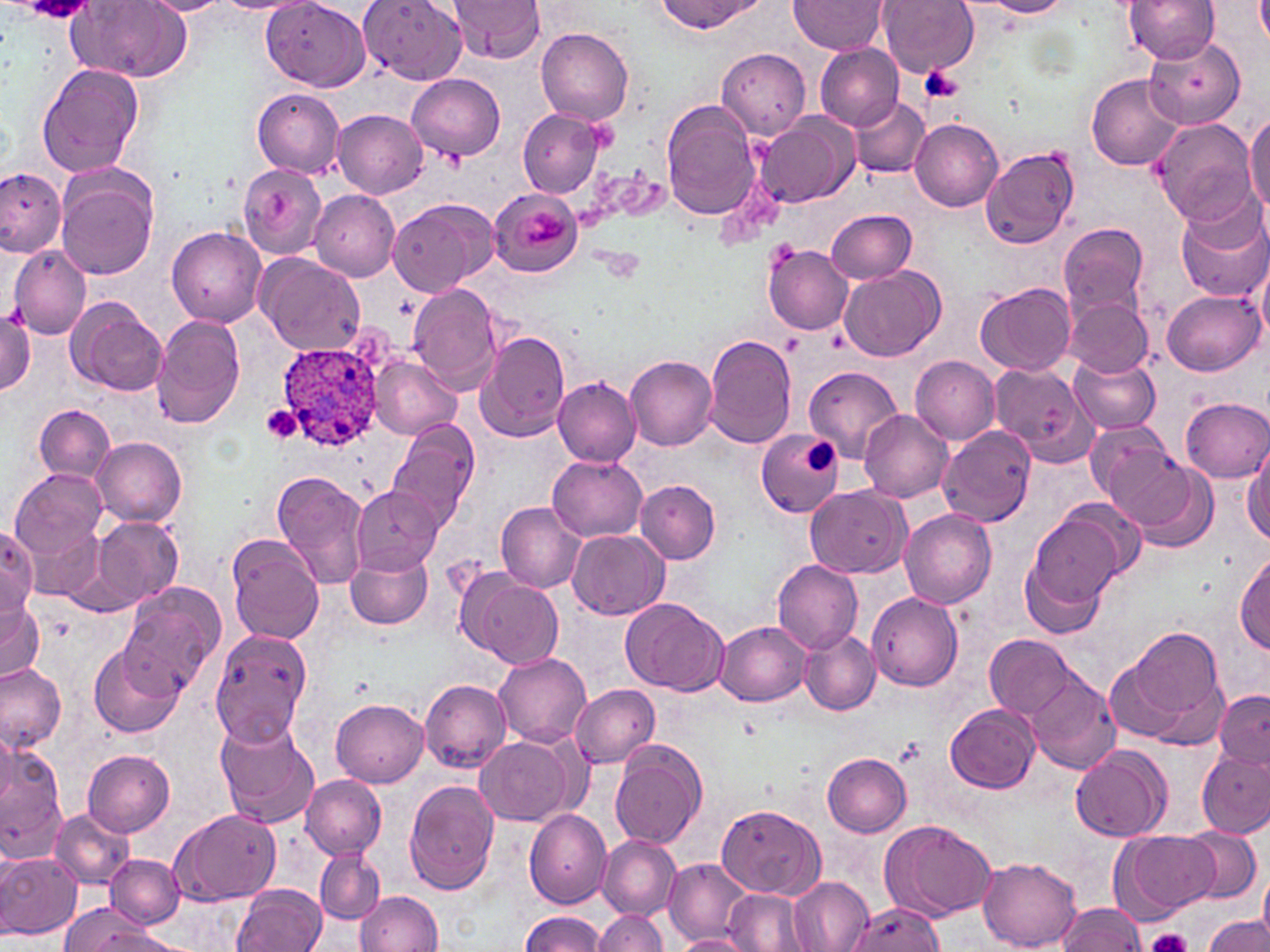

{
  "slide_level_diagnosis": "Plasmodium ovale",
  "stain": "May-Grünwald-Giemsa",
  "plasmodium_ovale_infected_red_blood_cell_locations": "approximate bounding boxes as (x1, y1, x2, y2) in pixels: (271, 339, 382, 450)",
  "uninfected_red_blood_cell_locations": "approximate bounding boxes as (x1, y1, x2, y2) in pixels: (66, 0, 194, 83), (138, 0, 230, 15), (262, 0, 370, 90), (360, 0, 466, 85), (448, 0, 544, 63), (656, 0, 757, 33), (788, 0, 889, 54), (877, 0, 978, 77), (979, 0, 1074, 17), (1122, 0, 1219, 62), (1257, 0, 1270, 49), (213, 1, 313, 12), (535, 27, 634, 124), (1144, 37, 1243, 128), (817, 44, 905, 131), (717, 48, 812, 138), (36, 63, 143, 177), (407, 71, 505, 163), (1086, 74, 1184, 170), (251, 86, 345, 179), (848, 96, 930, 177), (660, 101, 759, 220), (332, 109, 428, 198), (518, 109, 605, 197), (1245, 113, 1270, 216), (757, 114, 859, 210), (1149, 117, 1258, 225), (910, 118, 1004, 212), (979, 145, 1079, 249), (239, 162, 326, 258), (1, 166, 65, 257), (54, 169, 158, 278), (309, 187, 400, 282), (487, 188, 583, 277), (388, 197, 499, 295), (1176, 197, 1270, 302), (825, 208, 917, 283), (1058, 222, 1150, 323), (167, 226, 266, 326), (10, 244, 91, 339), (763, 245, 855, 335), (256, 254, 365, 357), (1256, 256, 1270, 350), (839, 265, 946, 361), (976, 282, 1076, 376), (407, 283, 505, 394), (1162, 286, 1265, 374), (1063, 295, 1153, 377), (65, 297, 168, 397), (1, 309, 36, 396), (153, 315, 247, 429), (476, 332, 571, 443), (704, 333, 797, 448), (1069, 352, 1161, 434), (370, 355, 463, 439), (626, 355, 718, 450), (912, 356, 1000, 445), (989, 363, 1092, 464), (803, 365, 903, 463), (554, 377, 642, 466), (1181, 396, 1270, 482), (33, 404, 116, 483), (859, 409, 955, 502), (386, 421, 480, 530), (1085, 421, 1178, 507), (937, 425, 1037, 527), (755, 427, 846, 518), (92, 434, 187, 526), (1243, 448, 1270, 546), (1112, 451, 1217, 551), (549, 456, 646, 541), (11, 469, 108, 576), (272, 470, 370, 590), (634, 478, 720, 564), (353, 485, 443, 574), (806, 485, 911, 578), (1055, 496, 1148, 586), (496, 501, 587, 593), (901, 508, 996, 610), (1029, 512, 1124, 607), (88, 515, 183, 612), (1, 529, 38, 616), (568, 530, 670, 620), (225, 535, 325, 646), (346, 547, 435, 630), (1235, 554, 1270, 655), (1022, 556, 1105, 639), (772, 559, 864, 654), (462, 574, 565, 670), (120, 583, 226, 700), (868, 592, 963, 691), (620, 597, 728, 696), (0, 600, 43, 685), (715, 620, 810, 706), (1110, 626, 1226, 739), (211, 629, 315, 748), (800, 630, 878, 715), (984, 634, 1075, 718), (90, 647, 181, 737), (495, 653, 592, 748), (0, 664, 66, 752), (1024, 670, 1120, 774), (419, 680, 512, 772), (569, 683, 660, 768), (1215, 690, 1269, 769), (330, 698, 428, 787), (946, 703, 1039, 794), (215, 717, 319, 829), (477, 737, 576, 826), (1, 740, 66, 864), (610, 740, 708, 848), (1070, 747, 1169, 843), (1196, 747, 1270, 838), (82, 750, 175, 835), (822, 753, 912, 836), (301, 775, 386, 858), (404, 778, 501, 896), (715, 804, 824, 898), (524, 808, 612, 908), (51, 810, 134, 888), (172, 811, 281, 904), (881, 819, 997, 919), (1112, 829, 1217, 920), (1182, 830, 1260, 903), (600, 836, 680, 919), (315, 848, 386, 924), (0, 852, 81, 940), (108, 854, 183, 927), (978, 856, 1082, 952), (665, 858, 754, 943), (1260, 864, 1269, 943), (787, 877, 873, 952), (233, 884, 326, 952), (723, 889, 808, 952), (359, 891, 441, 951), (1057, 902, 1144, 952), (845, 904, 947, 952), (59, 906, 178, 951), (592, 909, 667, 952), (519, 912, 607, 952), (1204, 914, 1269, 952), (76, 928, 187, 952), (674, 934, 752, 952)",
  "field_of_view": "one of a larger specimen",
  "modality": "optical microscopy",
  "preparation": "thin blood smear",
  "platelet_locations": "approximate bounding boxes as (x1, y1, x2, y2) in pixels: (19, 1, 96, 22), (921, 65, 964, 102), (584, 116, 620, 154), (767, 240, 801, 271), (260, 406, 301, 441), (799, 435, 841, 475), (1148, 927, 1194, 952)",
  "image_size": "1270×952 pixels",
  "magnification": "1000x"
}